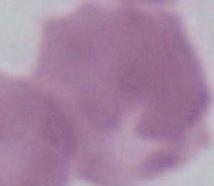
Summary:
  - Identification: erythrocyte
  - Magnification: 1000x
  - Modality: photomicrograph